Outline each uninfected red blood cell.
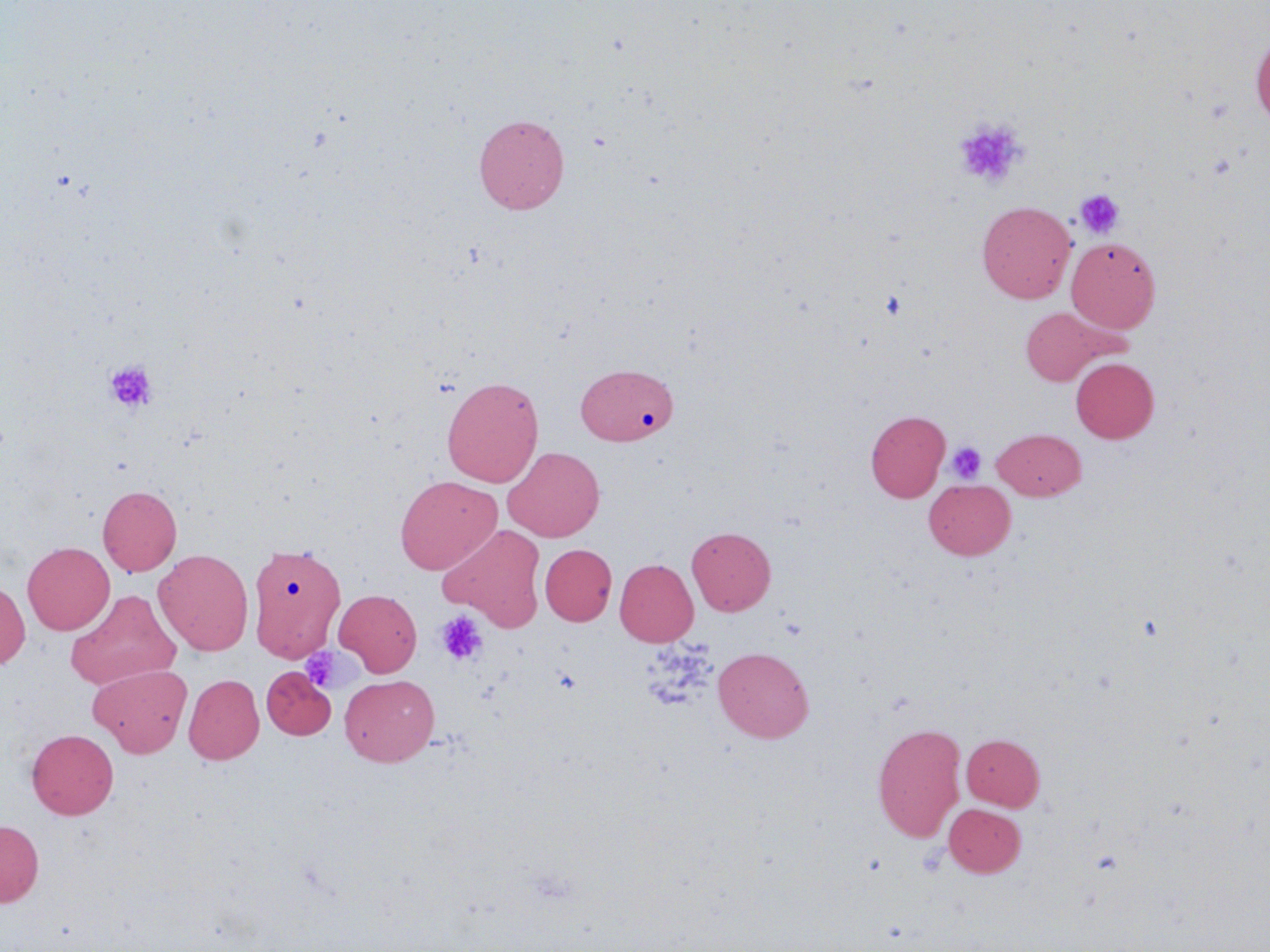

Approximate bounding boxes as named x1/y1/x2/y2 corners in pixels.
Uninfected red blood cells (subset): (x1=1250, y1=32, x2=1270, y2=127), (x1=474, y1=113, x2=570, y2=213), (x1=977, y1=201, x2=1076, y2=303), (x1=1066, y1=237, x2=1160, y2=332), (x1=1019, y1=306, x2=1118, y2=385), (x1=1071, y1=357, x2=1159, y2=443), (x1=575, y1=363, x2=678, y2=445), (x1=441, y1=376, x2=544, y2=487), (x1=865, y1=410, x2=950, y2=502), (x1=993, y1=428, x2=1086, y2=499), (x1=503, y1=446, x2=605, y2=542), (x1=395, y1=475, x2=501, y2=575), (x1=924, y1=479, x2=1016, y2=560), (x1=97, y1=485, x2=182, y2=576), (x1=439, y1=523, x2=547, y2=632), (x1=686, y1=526, x2=775, y2=616), (x1=22, y1=542, x2=114, y2=635), (x1=246, y1=544, x2=352, y2=666), (x1=539, y1=544, x2=616, y2=626), (x1=154, y1=549, x2=254, y2=655), (x1=614, y1=559, x2=698, y2=646), (x1=0, y1=578, x2=30, y2=669), (x1=334, y1=588, x2=422, y2=677), (x1=66, y1=590, x2=181, y2=690), (x1=713, y1=646, x2=814, y2=742), (x1=88, y1=664, x2=192, y2=757), (x1=183, y1=674, x2=264, y2=764), (x1=339, y1=674, x2=440, y2=766), (x1=872, y1=722, x2=967, y2=843), (x1=26, y1=729, x2=118, y2=819), (x1=961, y1=733, x2=1045, y2=810), (x1=943, y1=803, x2=1026, y2=877), (x1=0, y1=819, x2=44, y2=907).

Platelet locations (subset): (x1=953, y1=117, x2=1029, y2=189), (x1=1074, y1=189, x2=1125, y2=240), (x1=880, y1=289, x2=908, y2=321), (x1=104, y1=359, x2=158, y2=413), (x1=946, y1=441, x2=986, y2=483), (x1=435, y1=610, x2=488, y2=666), (x1=299, y1=647, x2=345, y2=692). Slide-level diagnosis: no evidence of blood parasites. Optical microscopy. Image is 1270×952 pixels. Thin blood film. May-Grünwald-Giemsa-stained preparation. Single field of view. 1000x magnification.